Describe the morphology of the erythrocytes.
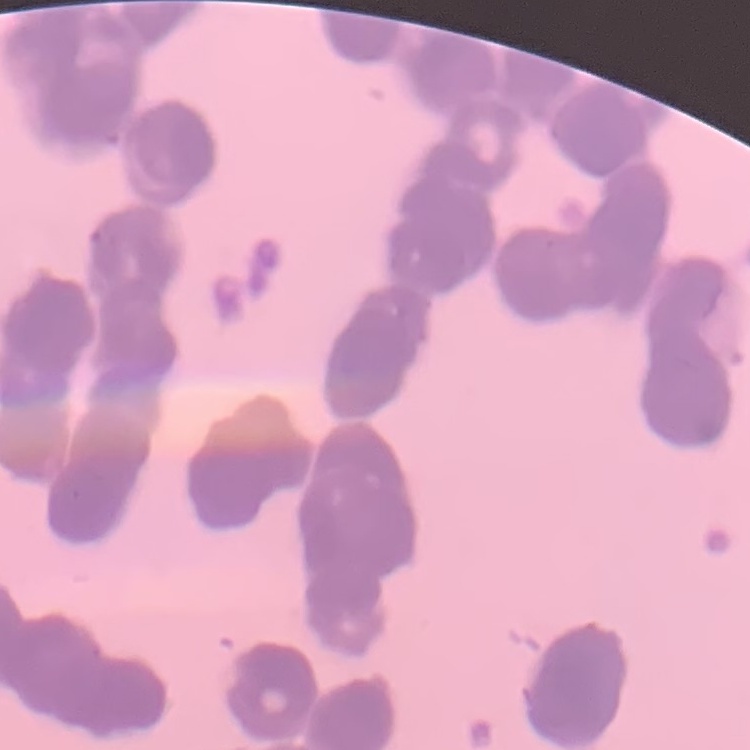

They show rouleaux formation.

Thin peripheral smear. Square crop of a larger photomicrograph. Field's or Giemsa stain.